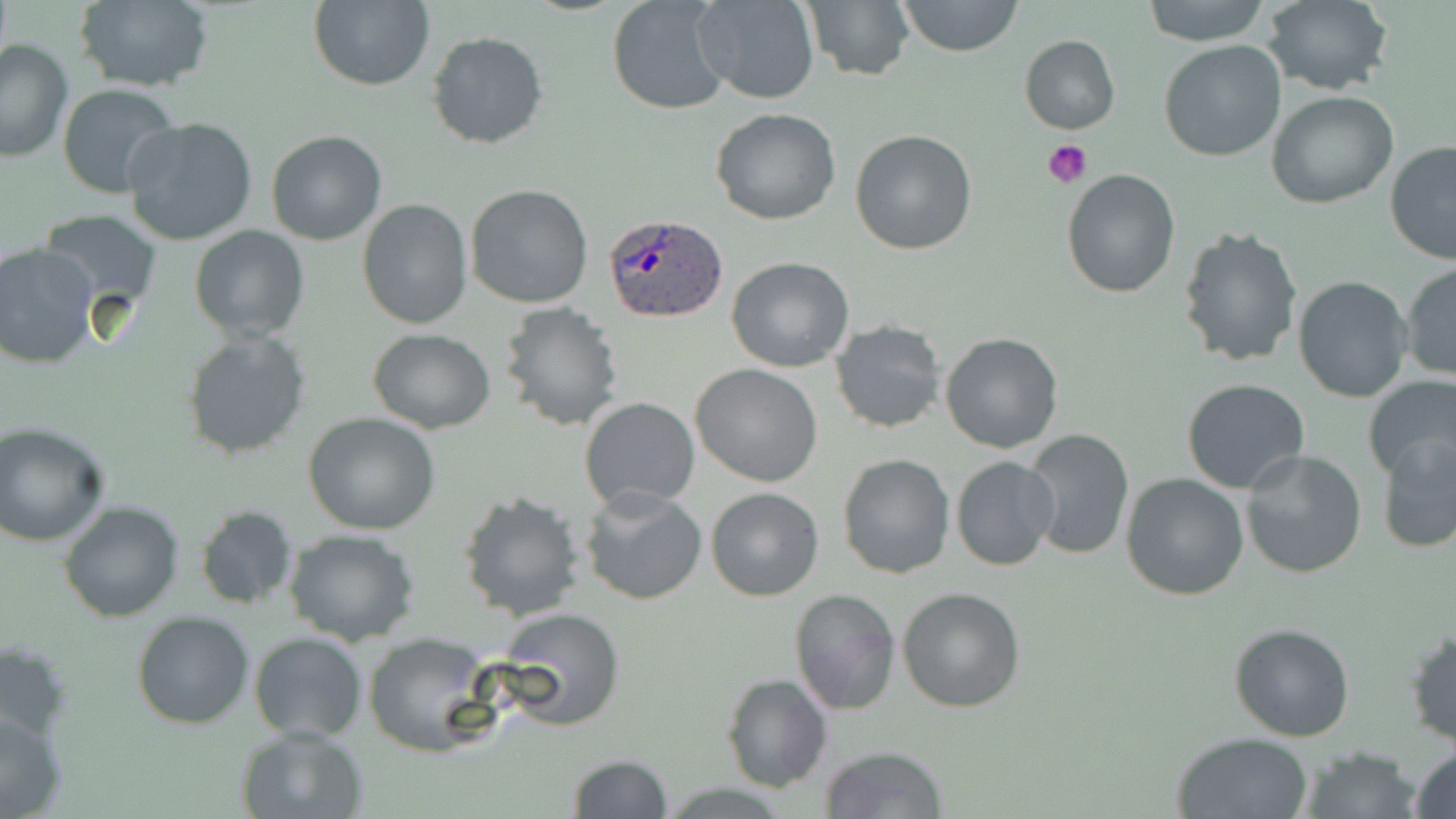

Approximate bounding boxes as named x1/y1/x2/y2 corners in pixels. Uninfected red blood cell locations: (x1=71, y1=0, x2=215, y2=91), (x1=306, y1=0, x2=435, y2=90), (x1=692, y1=0, x2=820, y2=104), (x1=897, y1=0, x2=1022, y2=58), (x1=1139, y1=0, x2=1274, y2=47), (x1=1260, y1=0, x2=1393, y2=94), (x1=603, y1=1, x2=728, y2=114), (x1=800, y1=1, x2=914, y2=82), (x1=427, y1=31, x2=548, y2=150), (x1=1019, y1=35, x2=1120, y2=134), (x1=0, y1=38, x2=74, y2=163), (x1=1157, y1=40, x2=1287, y2=163), (x1=58, y1=83, x2=182, y2=199), (x1=1267, y1=92, x2=1399, y2=209), (x1=710, y1=108, x2=841, y2=226), (x1=123, y1=117, x2=258, y2=246), (x1=849, y1=129, x2=977, y2=255), (x1=264, y1=130, x2=387, y2=246), (x1=1384, y1=140, x2=1456, y2=267), (x1=1061, y1=169, x2=1181, y2=298), (x1=464, y1=182, x2=594, y2=309), (x1=355, y1=199, x2=473, y2=330), (x1=41, y1=211, x2=163, y2=316), (x1=1176, y1=225, x2=1303, y2=369), (x1=189, y1=226, x2=310, y2=343), (x1=0, y1=241, x2=99, y2=370), (x1=726, y1=256, x2=854, y2=372), (x1=1401, y1=264, x2=1456, y2=381), (x1=1293, y1=275, x2=1413, y2=403), (x1=497, y1=302, x2=624, y2=431), (x1=829, y1=320, x2=947, y2=434), (x1=367, y1=328, x2=496, y2=432), (x1=181, y1=329, x2=313, y2=462), (x1=939, y1=331, x2=1063, y2=454), (x1=690, y1=363, x2=823, y2=485), (x1=1359, y1=373, x2=1456, y2=485), (x1=1181, y1=378, x2=1310, y2=493), (x1=580, y1=397, x2=701, y2=512), (x1=303, y1=411, x2=440, y2=535), (x1=0, y1=422, x2=111, y2=546), (x1=1022, y1=428, x2=1134, y2=559), (x1=1375, y1=432, x2=1456, y2=554), (x1=1239, y1=449, x2=1368, y2=579), (x1=836, y1=453, x2=955, y2=579), (x1=950, y1=456, x2=1060, y2=572), (x1=1120, y1=473, x2=1250, y2=601), (x1=580, y1=486, x2=708, y2=606), (x1=706, y1=487, x2=823, y2=602), (x1=457, y1=490, x2=587, y2=622), (x1=58, y1=499, x2=185, y2=622), (x1=194, y1=506, x2=300, y2=611), (x1=282, y1=527, x2=421, y2=646), (x1=898, y1=587, x2=1027, y2=713), (x1=790, y1=589, x2=901, y2=716), (x1=492, y1=606, x2=626, y2=729), (x1=132, y1=611, x2=255, y2=730), (x1=1229, y1=622, x2=1355, y2=742), (x1=1404, y1=626, x2=1455, y2=748), (x1=249, y1=633, x2=368, y2=742), (x1=363, y1=633, x2=495, y2=756), (x1=0, y1=639, x2=74, y2=744), (x1=721, y1=673, x2=832, y2=793), (x1=0, y1=706, x2=71, y2=816), (x1=236, y1=725, x2=370, y2=818), (x1=1171, y1=731, x2=1313, y2=819), (x1=819, y1=744, x2=948, y2=819), (x1=1301, y1=744, x2=1421, y2=819), (x1=1409, y1=744, x2=1456, y2=819), (x1=566, y1=754, x2=674, y2=819). Platelet locations: (x1=1043, y1=139, x2=1094, y2=191). Plasmodium ovale-infected red blood cell locations: (x1=605, y1=215, x2=728, y2=323). Slide-level diagnosis: Plasmodium ovale. May-Grünwald-Giemsa stain. Thin blood smear. One field of a larger specimen. Optical microscopy. 1000x magnification. Image is 1456×819 pixels.